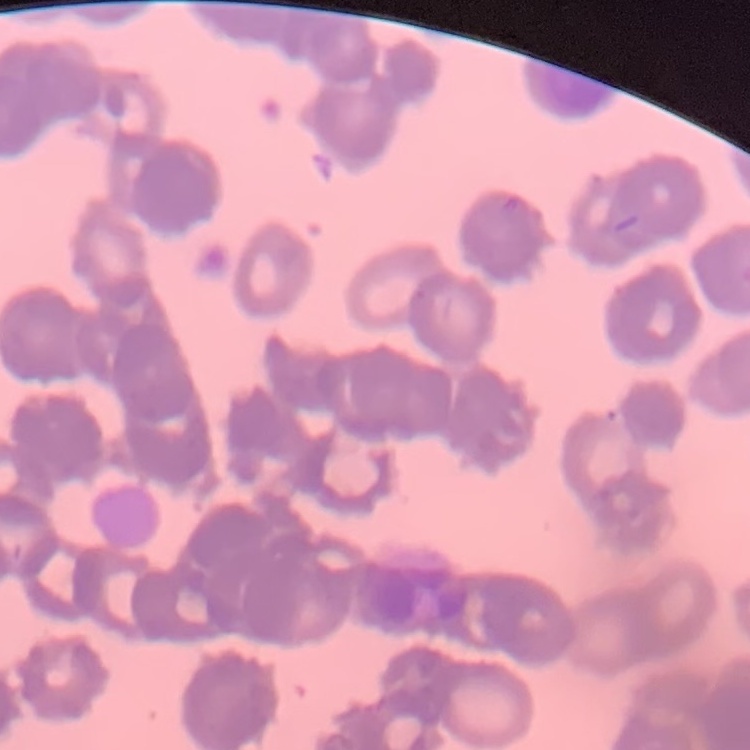

erythrocyte morphology = rouleaux formation
preparation = thin peripheral smear
image type = one tile cut from a larger photomicrograph
stain = Field's or Giemsa